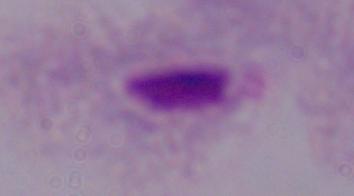

Summary:
  - Magnification: 1000x
  - Modality: micrograph
  - Identification: trichomonad